Assess this cell for malaria.
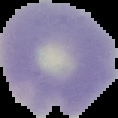
Uninfected.

Summary:
  - Image size: 118×118 pixels
  - Image type: segmented cell region on a black background
  - Preparation: thin blood smear